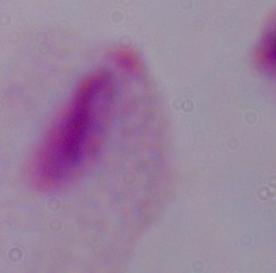 A trichomonad is shown. 1000x magnification. Photomicrograph.